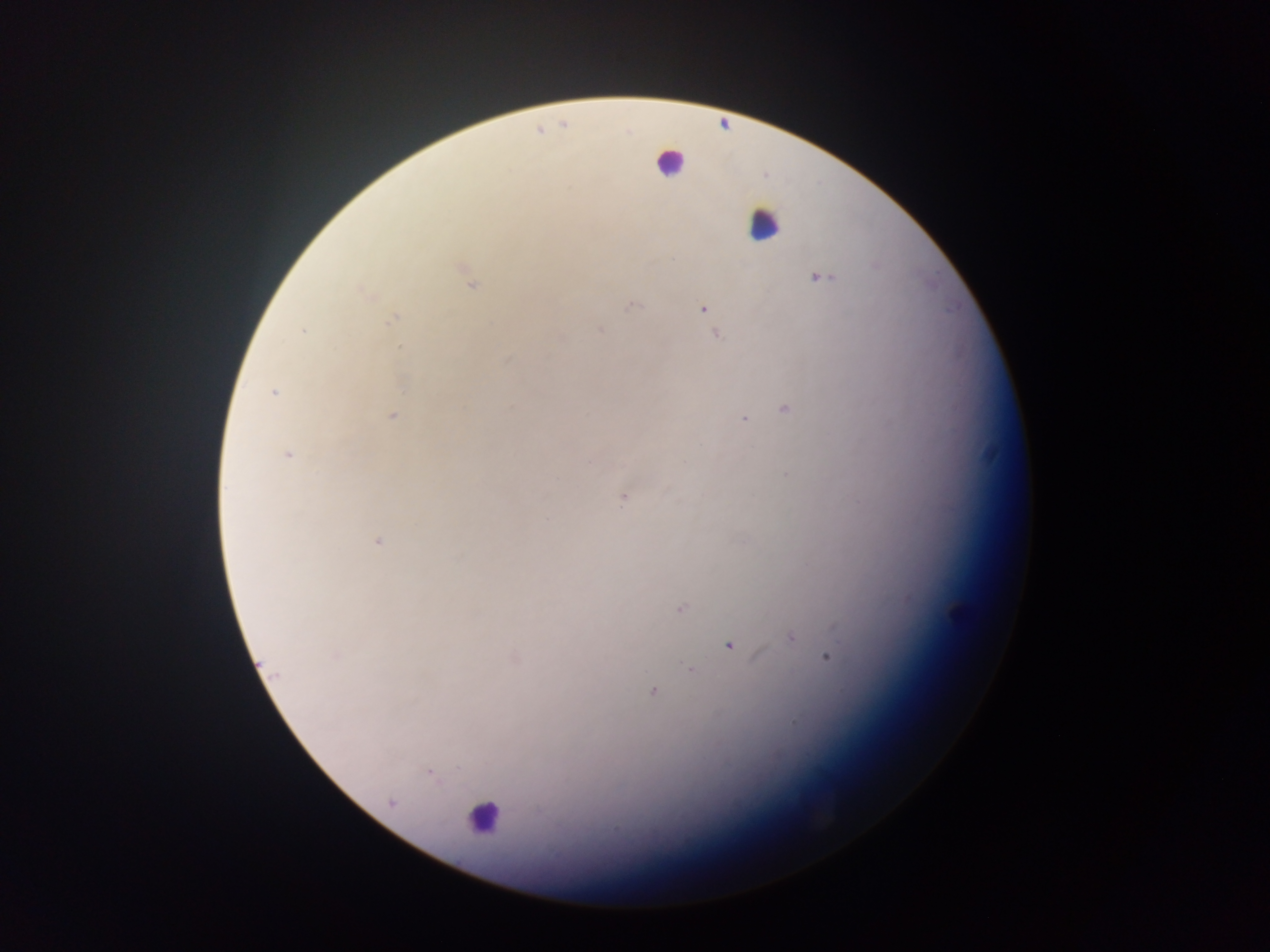

Approximate centers as {x, y} in pixels.
Summary:
  - Malaria parasite locations: {821, 278}, {470, 285}, {364, 292}, {631, 306}, {703, 308}, {392, 319}, {600, 330}, {303, 332}, {716, 335}, {400, 348}, {507, 359}, {404, 389}, {273, 393}, {785, 408}, {393, 416}, {744, 419}, {287, 454}, {590, 462}, {789, 475}, {623, 500}, {378, 541}, {680, 609}, {790, 638}, {730, 645}, {337, 655}, {827, 657}, {690, 669}, {652, 691}, {794, 722}, {428, 773}, {392, 802}
  - Leukocyte locations: {669, 162}, {763, 224}, {481, 818}
  - Capture: mobile-phone photograph through a microscope
  - Country: Ghana
  - Preparation: thick blood smear
  - Image size: 1270×952 pixels
  - Field of view: single